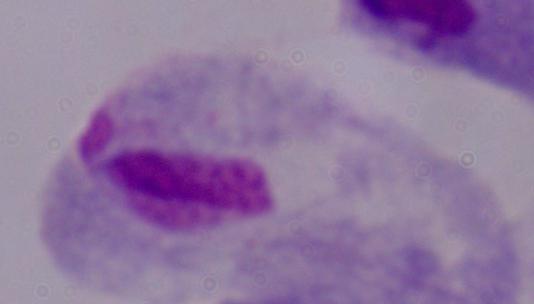

magnification = 1000x
identification = trichomonad
modality = micrograph